Report the malaria status of this cell.
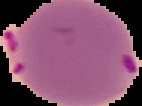

Parasitized.

From a thin blood film. Image is 142×106 pixels. Cell region segmented out of the field of view; the surrounding area is masked to black.